Assess this cell for malaria.
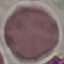

It is uninfected.

Giemsa-stained preparation. Photographed with a smartphone camera at the microscope eyepiece. Automatically extracted cell patch, resized to 64 × 64 pixels. Thin blood smear.